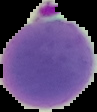

Summary:
  - Image type: cell region segmented out of the field of view; surrounding area masked to black
  - Image size: 97×112 pixels
  - Preparation: thin blood film
  - Malaria status: parasitized